Name the parasite shown.
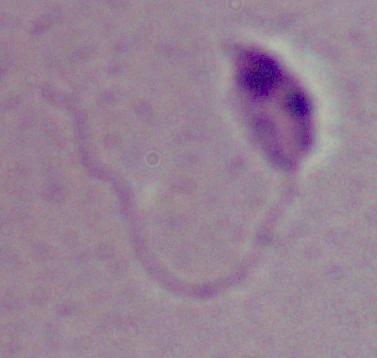
This is Leishmania.

Summary:
  - Magnification: 1000x
  - Modality: photomicrograph